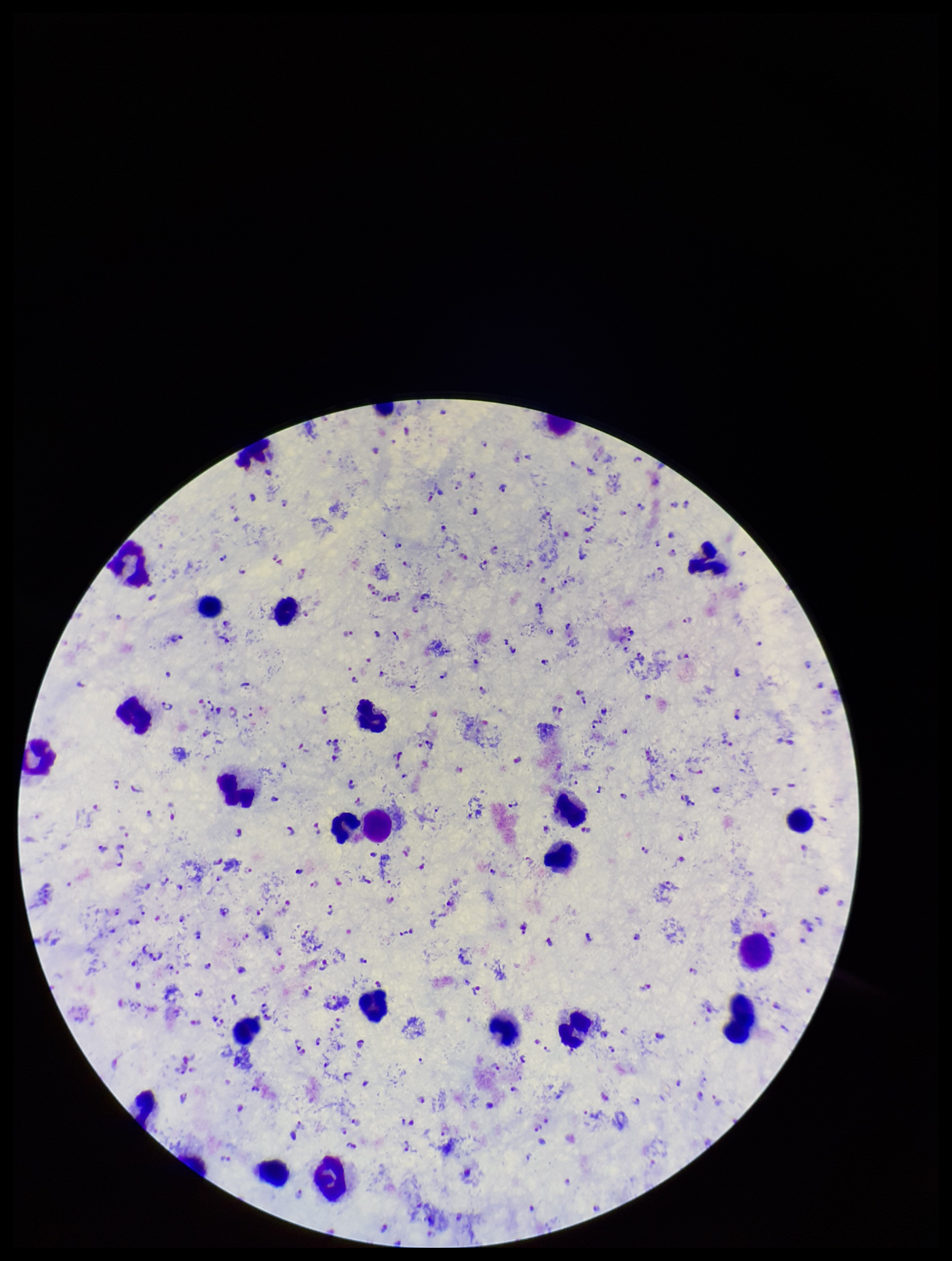

Summary:
  - Plasmodium parasites: identified
  - Preparation: thick
  - Leukocyte count: 25
  - Stain: Giemsa
  - Field of view: single
  - Patient malaria status: positive
  - Capture: smartphone photograph through the microscope eyepiece
  - Parasite count: 252
  - Image size: 952×1261 pixels
  - Species reported for this patient: Plasmodium falciparum